Assess this cell for malaria.
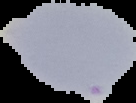

It is parasitized.

image size = 136×103 pixels
preparation = thin blood smear
image type = segmented cell region with the area outside set to black